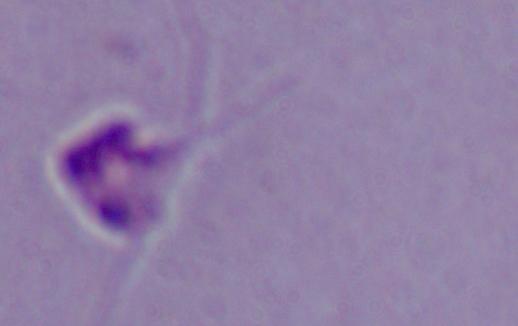

Summary:
  - Modality: photomicrograph
  - Magnification: 1000x
  - Identification: Leishmania